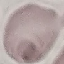

Summary:
  - Result: no malaria parasites detected
  - Preparation: thin blood smear
  - Stain: Giemsa
  - Image type: automatically extracted cell patch, resized to 64 × 64 pixels
  - Capture: smartphone camera at the microscope eyepiece